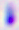
Summary:
  - Magnification: 400x
  - Identification: Toxoplasma gondii
  - Modality: micrograph